Name the cell type shown.
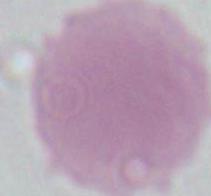
An erythrocyte.

Summary:
  - Modality: photomicrograph
  - Magnification: 1000x